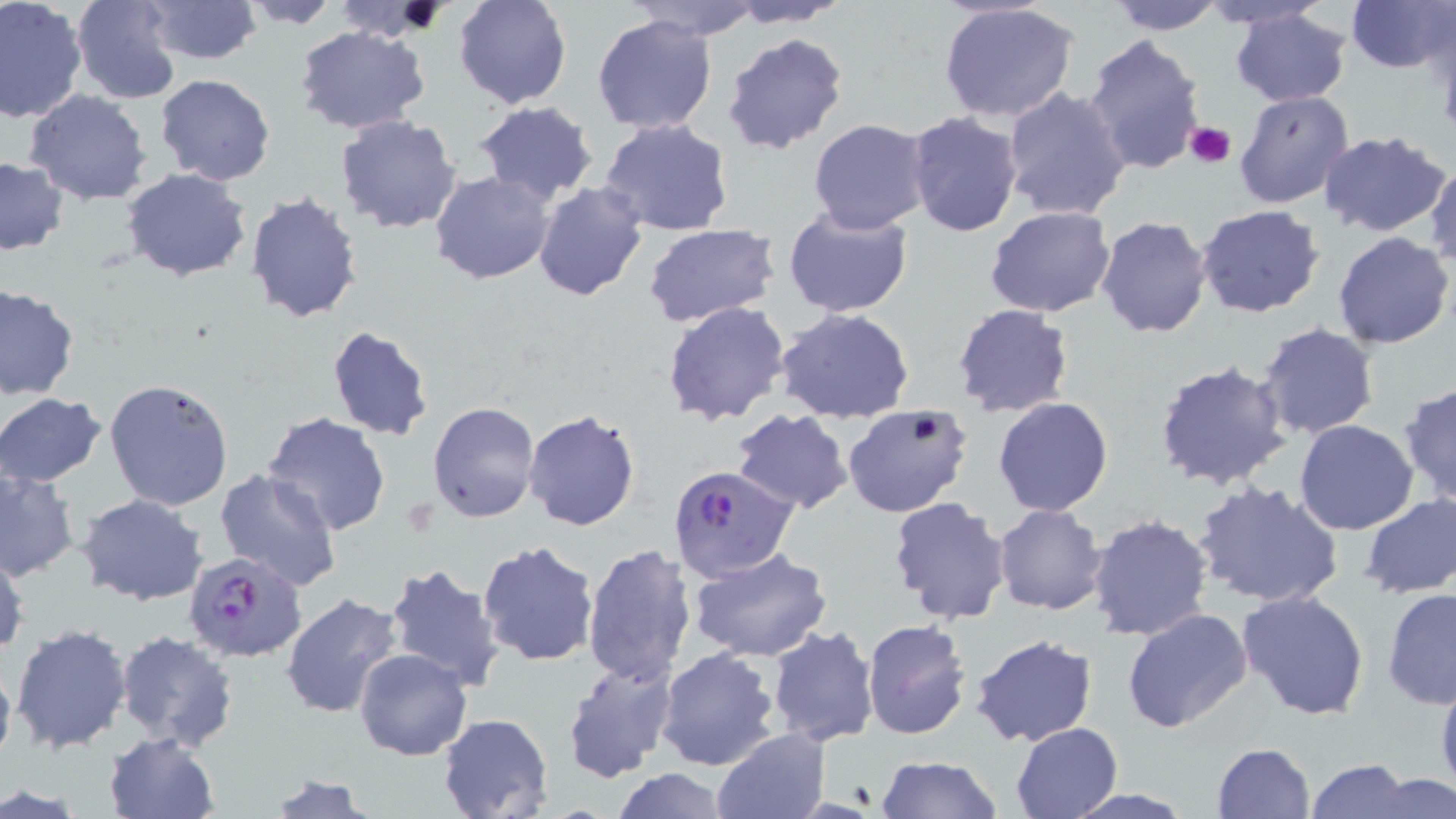

Summary:
  - Coordinate format: approximate bounding boxes as (x1, y1, x2, y2) in pixels
  - Platelet locations: (1184, 120, 1236, 167)
  - Uninfected red blood cell locations: (0, 0, 88, 122), (71, 0, 180, 103), (140, 0, 260, 65), (452, 0, 573, 110), (623, 0, 761, 39), (1196, 0, 1334, 30), (1345, 0, 1455, 73), (236, 1, 346, 29), (724, 1, 854, 26), (1105, 1, 1228, 35), (334, 2, 444, 43), (935, 2, 1081, 123), (0, 6, 159, 146), (1229, 8, 1352, 107), (591, 13, 718, 134), (294, 24, 431, 133), (722, 32, 850, 156), (1083, 33, 1208, 175), (153, 75, 275, 186), (1001, 85, 1132, 220), (25, 90, 152, 204), (1232, 90, 1355, 210), (472, 101, 599, 204), (905, 111, 1024, 237), (334, 115, 462, 234), (597, 118, 735, 238), (807, 118, 932, 234), (1318, 132, 1450, 237), (0, 157, 68, 254), (1426, 161, 1456, 268), (122, 168, 251, 280), (428, 170, 556, 284), (532, 183, 649, 301), (243, 190, 365, 324), (1195, 203, 1325, 317), (782, 205, 913, 317), (983, 205, 1115, 317), (1096, 216, 1213, 338), (641, 223, 782, 326), (1333, 232, 1453, 350), (0, 284, 78, 399), (661, 300, 791, 427), (950, 305, 1077, 419), (776, 309, 916, 424), (1257, 323, 1381, 439), (324, 324, 435, 443), (1151, 356, 1294, 492), (104, 378, 235, 511), (1399, 379, 1456, 506), (0, 393, 107, 488), (992, 396, 1113, 516), (427, 401, 539, 522), (843, 404, 974, 519), (523, 409, 640, 532), (732, 409, 854, 512), (261, 412, 392, 537), (1294, 418, 1419, 535), (0, 469, 80, 580), (213, 470, 343, 593), (1192, 481, 1345, 609), (1359, 491, 1456, 598), (75, 494, 207, 607), (887, 497, 1012, 627), (994, 505, 1107, 616), (1086, 513, 1214, 640), (477, 540, 599, 667), (581, 543, 698, 690), (687, 547, 834, 662), (1, 549, 28, 658), (384, 561, 506, 693), (1381, 588, 1456, 708), (1236, 591, 1370, 720), (281, 593, 405, 720), (1122, 607, 1253, 734), (862, 619, 971, 738), (10, 622, 132, 757), (766, 625, 880, 748), (113, 632, 240, 753), (970, 635, 1097, 748), (656, 646, 781, 771), (354, 647, 472, 761), (0, 653, 16, 776), (561, 657, 678, 782), (1434, 666, 1456, 805), (437, 713, 554, 819), (1010, 722, 1125, 817), (712, 728, 832, 819), (104, 732, 218, 818), (1210, 740, 1317, 817), (875, 756, 1005, 818), (1305, 758, 1413, 819), (612, 767, 732, 819), (1366, 771, 1455, 819), (260, 773, 378, 819), (1059, 788, 1199, 818)
  - Plasmodium falciparum-infected red blood cell locations: (669, 465, 797, 582), (185, 550, 308, 661)
  - Slide-level diagnosis: Plasmodium falciparum
  - Modality: light microscopy
  - Image size: 1456×819 pixels
  - Magnification: 1000x
  - Preparation: thin blood smear
  - Field of view: single
  - Stain: May-Grünwald-Giemsa